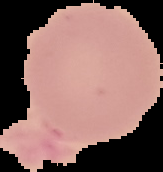

preparation: thin blood smear
result: no Plasmodium parasites seen
image_size: 163×172 pixels
image_type: segmented cell region with the area outside set to black